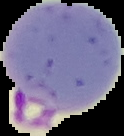
From a thin blood smear. Image is 124×136 pixels. Malaria status: parasitized. Segmented cell region on a black background.